Locate every Plasmodium ovale-infected red blood cell.
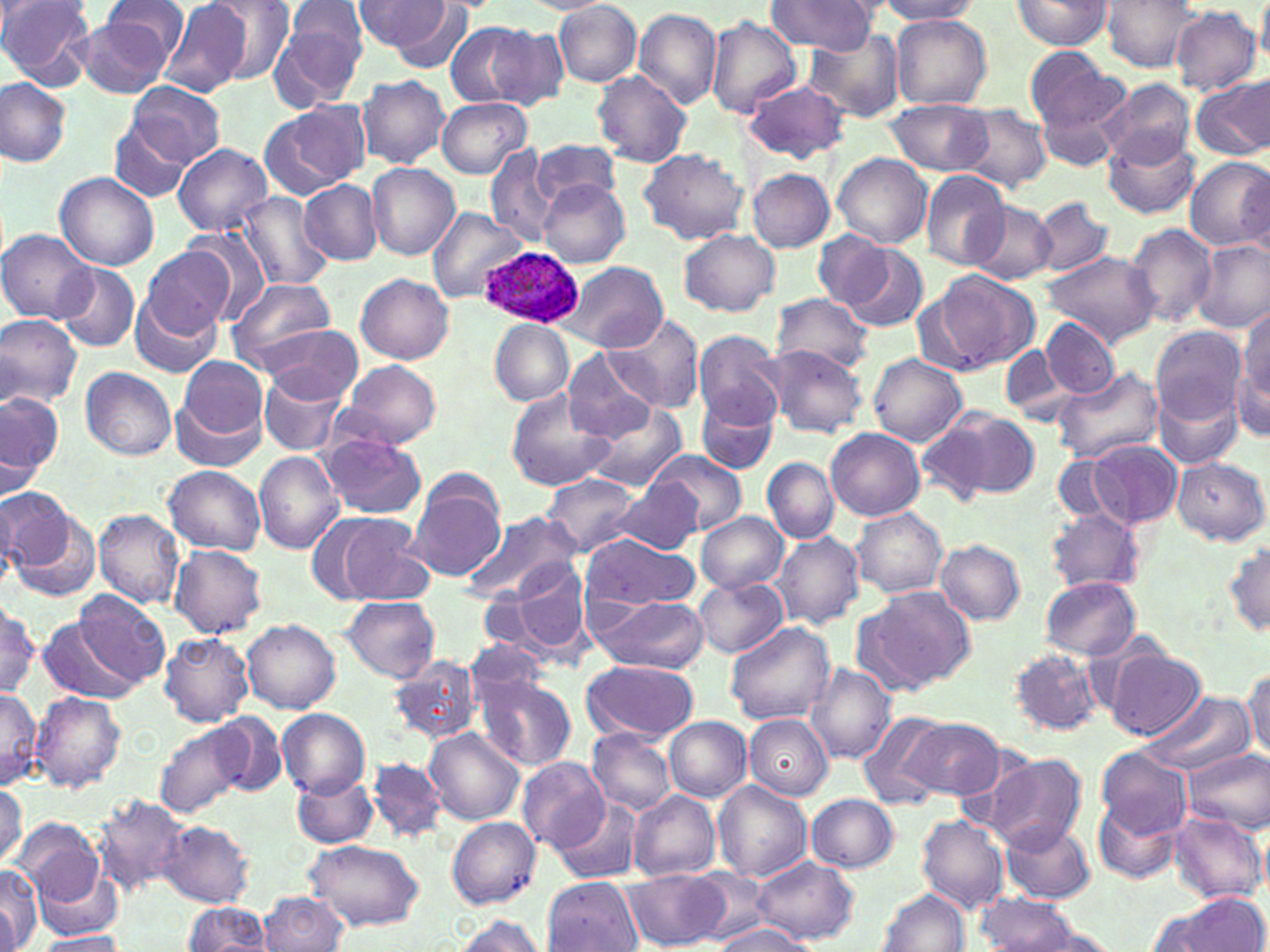

Approximate bounding boxes as (x1,y1)-(x2,y2) corner pairs in pixels.
Plasmodium ovale-infected red blood cells: (478,248)-(585,329).

Uninfected red blood cell locations: (0,0)-(95,88), (102,0)-(188,73), (161,0)-(255,96), (204,0)-(297,82), (351,0)-(452,53), (768,0)-(877,55), (879,0)-(981,24), (1100,0)-(1202,71), (1009,1)-(1112,52), (1257,2)-(1270,71), (383,3)-(473,72), (555,4)-(642,85), (271,5)-(366,109), (1170,7)-(1261,96), (632,8)-(722,110), (76,12)-(177,99), (707,15)-(802,118), (891,16)-(992,109), (445,21)-(544,108), (487,25)-(573,112), (804,33)-(906,121), (1024,45)-(1126,134), (593,71)-(693,167), (357,74)-(450,169), (1190,76)-(1270,160), (0,77)-(71,167), (1100,78)-(1196,168), (744,79)-(850,163), (127,82)-(224,166), (1035,91)-(1127,171), (437,97)-(532,179), (885,99)-(991,177), (259,102)-(369,200), (956,104)-(1049,190), (109,120)-(194,203), (1103,131)-(1203,220), (531,140)-(623,210), (172,143)-(274,237), (484,146)-(560,249), (639,148)-(748,246), (833,153)-(933,247), (1184,156)-(1270,252), (366,163)-(460,260), (747,169)-(834,253), (920,170)-(1011,269), (54,174)-(159,271), (299,179)-(383,264), (539,181)-(629,267), (234,191)-(333,292), (1031,195)-(1114,276), (967,200)-(1056,284), (429,208)-(526,303), (1124,222)-(1216,328), (180,227)-(277,326), (1,229)-(100,325), (680,229)-(779,317), (815,230)-(895,309), (1194,239)-(1268,332), (141,244)-(236,338), (839,244)-(929,332), (1042,252)-(1158,345), (558,261)-(667,352), (56,264)-(140,352), (921,269)-(1038,373), (357,274)-(454,364), (225,278)-(338,370), (128,282)-(225,379), (773,293)-(877,373), (1237,306)-(1270,417), (0,313)-(82,410), (605,313)-(704,413), (1042,317)-(1120,397), (488,319)-(574,405), (264,324)-(362,402), (1151,325)-(1246,424), (691,330)-(785,429), (1000,344)-(1073,421), (764,345)-(869,437), (562,350)-(659,443), (176,354)-(269,450), (869,355)-(966,447), (339,359)-(443,450), (1232,360)-(1269,438), (1051,366)-(1164,464), (80,367)-(177,460), (258,370)-(347,456), (1153,379)-(1245,469), (505,389)-(617,493), (0,391)-(62,481), (697,392)-(780,475), (171,395)-(264,471), (586,403)-(686,491), (931,407)-(1041,502), (912,421)-(993,509), (826,429)-(925,522), (319,435)-(426,519), (1085,440)-(1182,529), (647,449)-(748,535), (254,451)-(344,554), (1054,455)-(1119,521), (1171,457)-(1267,546), (762,458)-(839,543), (164,466)-(266,555), (543,474)-(643,556), (408,477)-(505,582), (609,478)-(704,557), (0,488)-(72,570), (0,496)-(20,593), (852,507)-(949,597), (93,509)-(184,609), (1046,509)-(1146,592), (462,510)-(580,603), (7,511)-(105,605), (696,512)-(789,592), (328,513)-(434,606), (772,531)-(865,630), (578,534)-(700,612), (935,539)-(1026,624), (1223,539)-(1270,637), (171,545)-(266,638), (501,557)-(595,661), (694,575)-(787,658), (1039,576)-(1142,659), (856,586)-(974,693), (75,592)-(171,687), (588,594)-(708,673), (339,596)-(441,683), (0,600)-(40,701), (41,617)-(138,703), (242,619)-(340,714), (725,621)-(835,726), (160,633)-(254,728), (465,641)-(548,711), (1008,648)-(1104,737), (1105,650)-(1204,740), (387,655)-(481,744), (581,660)-(699,742), (806,663)-(897,764), (1244,666)-(1270,759), (477,673)-(575,769), (0,688)-(40,790), (29,691)-(125,792), (1138,692)-(1253,776), (277,708)-(370,797), (857,712)-(955,811), (215,713)-(286,797), (744,714)-(832,799), (664,716)-(751,802), (904,717)-(1002,800), (153,723)-(248,819), (424,728)-(524,826), (589,729)-(675,814), (1182,749)-(1270,833), (1096,751)-(1193,840), (985,753)-(1088,853), (367,757)-(446,842), (517,757)-(609,850), (293,773)-(377,848), (714,780)-(812,882), (0,781)-(26,869), (629,791)-(721,881), (806,793)-(899,872), (94,795)-(191,897), (554,796)-(644,883), (1093,797)-(1183,885), (1169,813)-(1267,903), (916,814)-(1010,912), (446,817)-(542,909), (12,818)-(111,921), (999,819)-(1096,904), (158,820)-(255,908), (303,840)-(425,930), (750,855)-(859,944), (0,864)-(40,952), (627,869)-(728,950), (543,877)-(641,951), (877,887)-(969,952), (258,891)-(348,952), (975,891)-(1086,950), (1167,892)-(1268,952), (183,901)-(272,951), (1145,905)-(1221,951), (451,915)-(544,952), (710,918)-(816,952), (32,931)-(127,952). Slide-level diagnosis: Plasmodium ovale. Image is 1270×952 pixels. May-Grünwald-Giemsa stain. Thin blood smear. Captured at 1000x magnification. Single field of view. Light microscopy.